Name the blood parasite species.
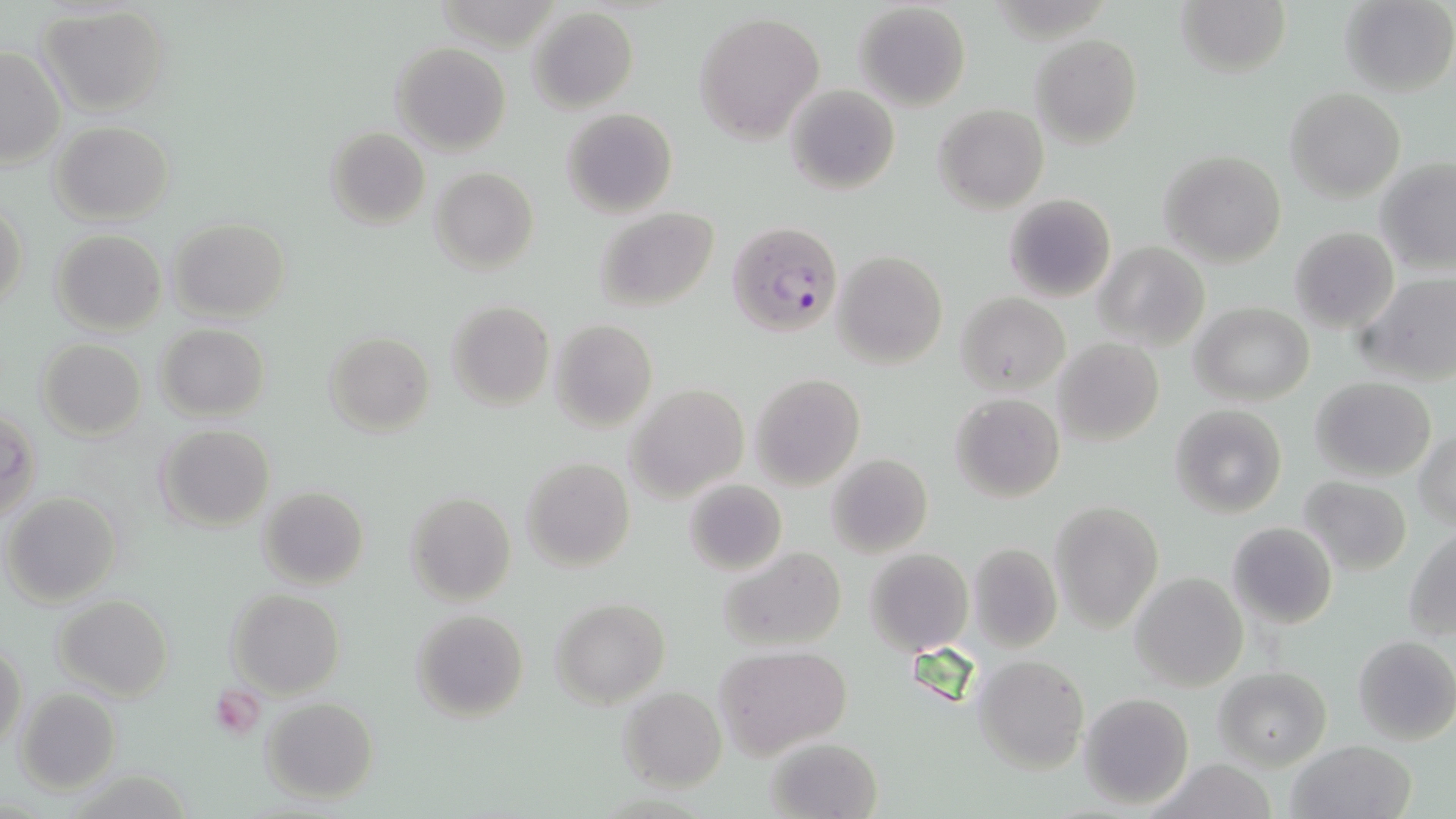
Plasmodium falciparum.

Summary:
  - Coordinate format: approximate bounding boxes as (x1,y1)-(x2,y2) corner pairs in pixels
  - Plasmodium falciparum-infected red blood cell locations: (727,220)-(845,340)
  - Platelet locations: (210,686)-(266,739)
  - Uninfected red blood cell locations: (1174,0)-(1291,79), (1340,0)-(1455,96), (853,1)-(972,112), (36,5)-(173,117), (527,7)-(639,113), (693,11)-(825,144), (1031,33)-(1143,147), (390,41)-(511,155), (0,45)-(66,167), (785,84)-(900,196), (1285,87)-(1405,203), (934,103)-(1049,213), (561,107)-(677,218), (50,120)-(175,225), (325,126)-(431,229), (1159,150)-(1285,267), (1375,157)-(1456,275), (430,166)-(539,274), (1003,193)-(1116,302), (0,201)-(29,314), (595,207)-(721,312), (170,218)-(290,323), (1289,226)-(1398,334), (51,229)-(167,335), (1095,241)-(1209,350), (833,249)-(947,370), (1359,271)-(1456,384), (956,293)-(1068,393), (446,301)-(554,411), (1192,302)-(1314,407), (550,319)-(658,432), (155,323)-(270,421), (323,331)-(434,437), (36,338)-(147,439), (1054,338)-(1164,446), (752,374)-(865,491), (1310,376)-(1438,480), (627,383)-(749,502), (951,393)-(1066,503), (1168,404)-(1287,518), (1,410)-(40,524), (156,425)-(275,532), (1415,429)-(1456,527), (826,454)-(932,558), (521,456)-(634,571), (1299,476)-(1412,576), (684,478)-(787,577), (259,486)-(369,590), (3,491)-(123,606), (404,491)-(517,606), (1052,500)-(1161,631), (1228,522)-(1337,630), (1404,528)-(1456,639), (965,542)-(1062,652), (719,546)-(848,655), (865,548)-(972,655), (1130,572)-(1248,691), (227,589)-(344,697), (56,594)-(172,702), (550,598)-(669,707), (411,609)-(530,723), (1353,635)-(1456,745), (1,640)-(26,751), (715,645)-(853,757), (973,654)-(1090,773), (1213,666)-(1332,770), (617,686)-(727,791), (14,688)-(121,793), (1079,691)-(1194,811), (260,696)-(377,804), (768,736)-(884,818), (1286,738)-(1417,819), (1150,757)-(1280,819)
  - Modality: light microscopy
  - Field of view: single
  - Stain: May-Grünwald-Giemsa
  - Preparation: thin blood smear
  - Image size: 1456×819 pixels
  - Magnification: 1000x